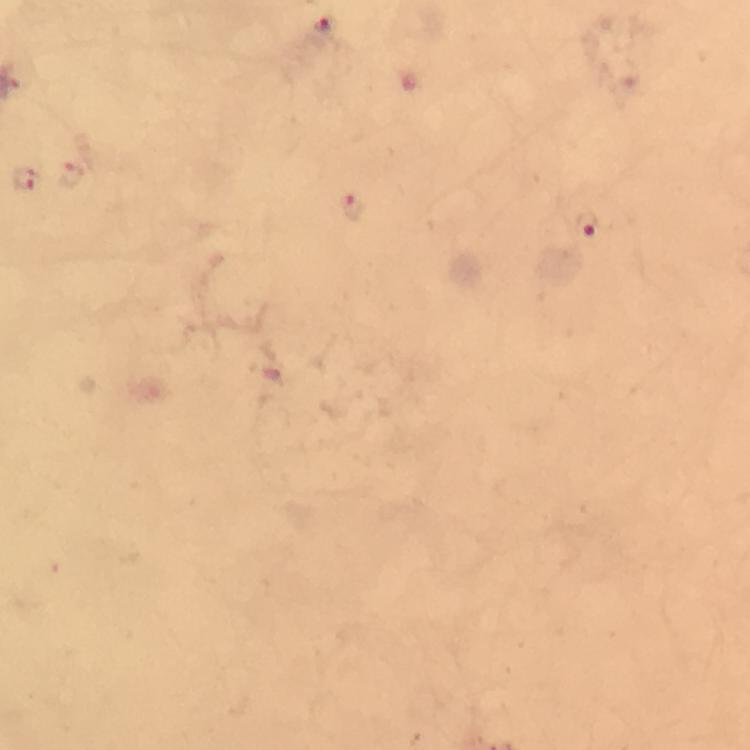

Approximate centers as [x, y] in pixels. Plasmodium parasite locations: [324, 26], [27, 179], [354, 209], [588, 225]. Photographed with a smartphone mounted on the microscope. From a diagnostic examination for malaria. Giemsa stain. Image is 750×750 pixels. A crop from one field of view. At 100x magnification. Thick smear. Immersion oil applied.